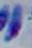 Captured at 1000x magnification. Photomicrograph. Toxoplasma gondii is seen.